Identify the cell.
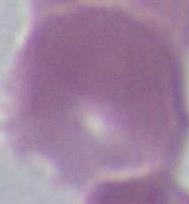
An erythrocyte.

Summary:
  - Magnification: 1000x
  - Modality: photomicrograph